Outline each blood parasite and name the species.
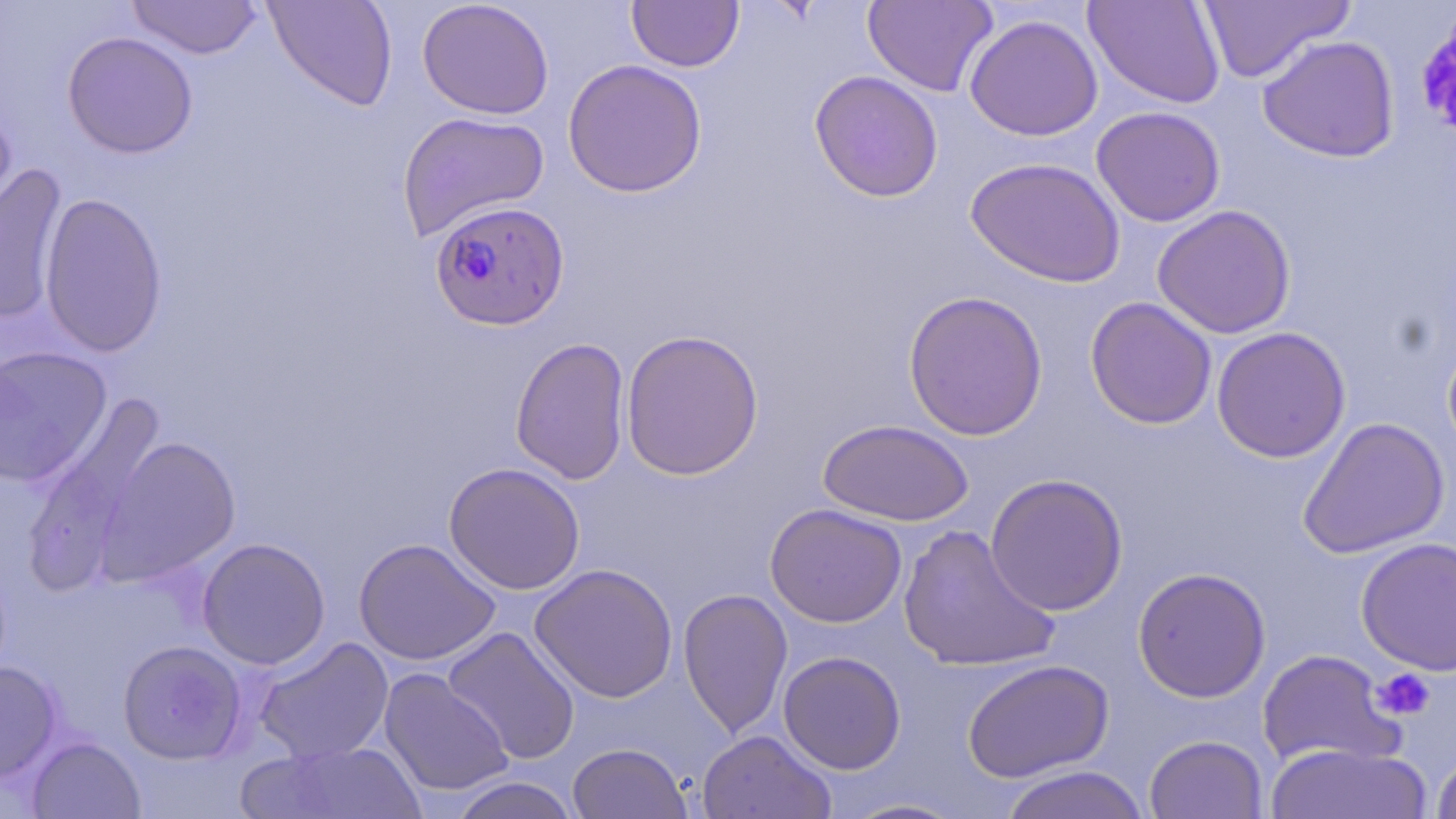

Approximate bounding boxes as (x1, y1, x2, y2) in pixels.
Plasmodium falciparum-infected red blood cells: (429, 200, 569, 331).
No Plasmodium ovale, Plasmodium malariae, Plasmodium vivax, Babesia divergens, or Trypanosoma brucei observed.

Uninfected red blood cell locations: (127, 0, 263, 59), (263, 0, 399, 112), (417, 0, 555, 120), (863, 0, 998, 97), (1083, 0, 1227, 109), (1196, 0, 1352, 83), (627, 1, 744, 72), (964, 14, 1104, 141), (62, 31, 199, 159), (1257, 35, 1400, 162), (562, 59, 708, 198), (809, 70, 944, 202), (0, 100, 17, 232), (1090, 106, 1226, 227), (396, 111, 550, 241), (965, 157, 1127, 287), (0, 162, 69, 327), (39, 191, 168, 358), (1152, 204, 1296, 339), (903, 290, 1048, 441), (1084, 297, 1217, 430), (1211, 326, 1351, 463), (620, 329, 764, 480), (510, 337, 631, 485), (0, 345, 112, 488), (19, 395, 169, 594), (1296, 416, 1451, 559), (818, 419, 974, 526), (95, 435, 241, 586), (443, 462, 586, 595), (985, 473, 1128, 616), (764, 503, 907, 628), (897, 524, 1059, 673), (196, 537, 331, 670), (1355, 537, 1456, 675), (353, 538, 501, 666), (529, 563, 679, 703), (1132, 567, 1271, 703), (678, 588, 794, 738), (441, 626, 581, 765), (253, 637, 395, 765), (118, 640, 247, 764), (1257, 649, 1404, 769), (778, 651, 906, 774), (962, 659, 1114, 783), (0, 661, 62, 781), (378, 668, 513, 798), (696, 729, 836, 819), (1144, 734, 1268, 819), (26, 736, 145, 819), (250, 741, 428, 819), (567, 742, 692, 818), (1266, 742, 1433, 819), (1430, 749, 1456, 818), (999, 765, 1150, 819), (447, 776, 582, 819), (836, 797, 970, 818). Platelet locations: (1371, 668, 1435, 722). Slide-level diagnosis: Plasmodium falciparum. Image is 1456×819 pixels. Single field of view. 1000x magnification. May-Grünwald-Giemsa-stained preparation. Thin blood smear. Light microscopy.